Assess this cell for malaria.
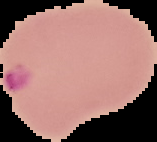
It is parasitized.

image_size: 157×142 pixels
image_type: segmented cell region with the area outside set to black
preparation: thin blood film